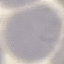

Summary:
  - Result: negative for malaria parasites
  - Image type: cell patch, automatically extracted from a larger field of view and resized to 64 × 64 pixels
  - Capture: smartphone through the microscope eyepiece
  - Stain: Giemsa
  - Preparation: thin blood film